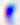
400x magnification. Photomicrograph. Toxoplasma gondii is shown.